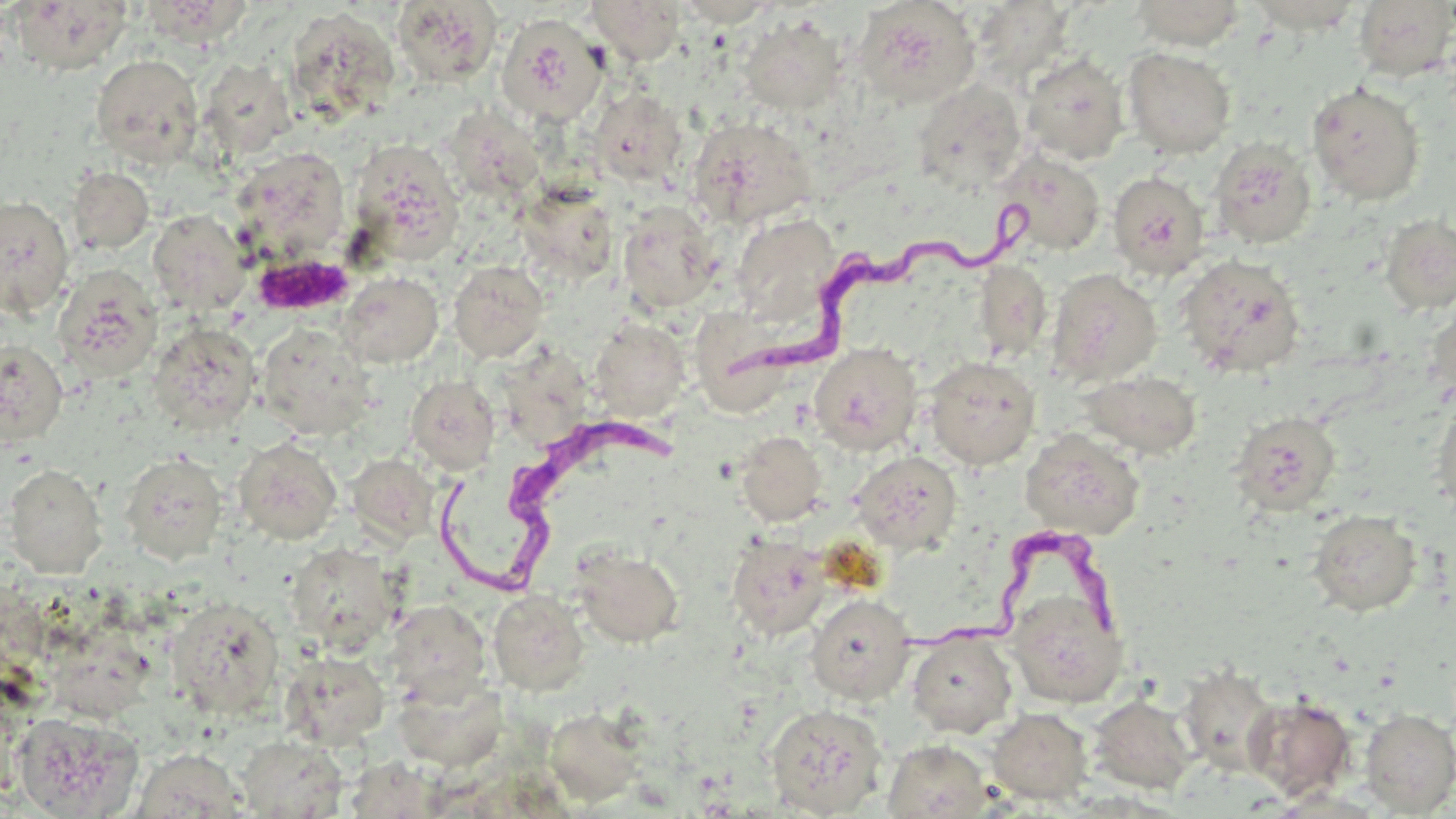

Summary:
  - Coordinate format: approximate bounding boxes as [x1, y1, x2, y2] in pixels
  - Trypanosoma brucei locations: [724, 192, 1038, 379], [441, 406, 690, 607], [897, 532, 1129, 671]
  - Uninfected red blood cell locations: [9, 0, 134, 74], [141, 0, 253, 46], [588, 0, 684, 64], [853, 0, 980, 108], [972, 0, 1075, 84], [1129, 0, 1247, 49], [392, 1, 501, 87], [1352, 1, 1456, 81], [285, 7, 399, 124], [496, 14, 608, 126], [738, 15, 849, 115], [1123, 47, 1236, 158], [1021, 53, 1129, 164], [91, 54, 204, 167], [200, 60, 296, 159], [913, 79, 1027, 193], [1306, 80, 1425, 206], [589, 87, 688, 188], [445, 109, 547, 202], [686, 116, 817, 228], [1208, 138, 1317, 250], [348, 140, 464, 263], [229, 146, 351, 263], [994, 149, 1107, 257], [68, 167, 154, 254], [1107, 172, 1211, 278], [516, 181, 619, 284], [0, 195, 75, 317], [617, 201, 721, 314], [148, 209, 251, 316], [731, 213, 841, 325], [1379, 214, 1456, 315], [1176, 254, 1306, 379], [973, 259, 1052, 360], [448, 260, 549, 363], [54, 265, 162, 382], [1047, 268, 1162, 387], [337, 271, 443, 368], [682, 297, 790, 423], [1426, 300, 1456, 406], [589, 318, 690, 421], [147, 322, 260, 433], [257, 322, 376, 439], [0, 340, 68, 445], [808, 343, 922, 455], [924, 356, 1041, 469], [1081, 370, 1202, 458], [405, 375, 500, 474], [1432, 395, 1456, 520], [1230, 411, 1341, 515], [1020, 428, 1144, 539], [736, 431, 826, 525], [234, 437, 342, 544], [850, 450, 963, 553], [120, 453, 227, 564], [348, 454, 439, 544], [3, 463, 107, 577], [1307, 510, 1422, 616], [727, 534, 831, 640], [286, 542, 402, 655], [572, 546, 684, 648], [1006, 588, 1128, 708], [489, 590, 590, 695], [806, 594, 915, 704], [166, 597, 284, 719], [384, 599, 491, 704], [906, 631, 1017, 738], [281, 651, 390, 749], [1178, 662, 1281, 776], [394, 673, 507, 770], [1089, 694, 1196, 794], [1246, 695, 1357, 801], [765, 703, 888, 817], [544, 707, 647, 807], [986, 707, 1092, 804], [1359, 708, 1456, 816], [13, 711, 144, 818], [236, 735, 349, 818], [883, 740, 992, 819], [133, 748, 247, 818]
  - Platelet locations: [252, 252, 356, 317]
  - Slide-level diagnosis: Trypanosoma brucei
  - Field of view: one of a larger specimen
  - Preparation: thin blood film
  - Modality: light microscopy
  - Magnification: 1000x
  - Image size: 1456×819 pixels
  - Stain: May-Grünwald-Giemsa